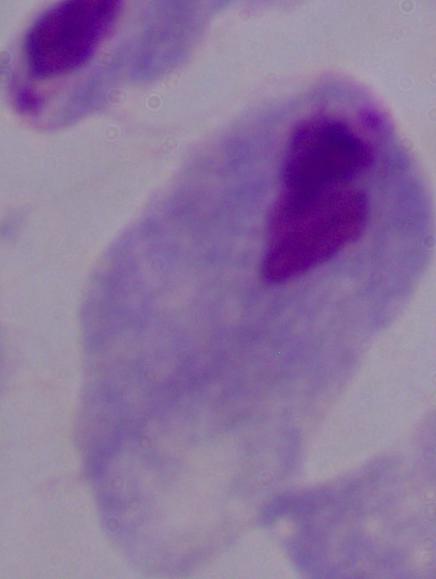
Summary:
  - Modality: micrograph
  - Identification: trichomonad
  - Magnification: 1000x